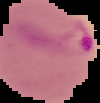
preparation = thin blood smear
image type = cell region segmented out of the field of view; surrounding area masked to black
image size = 100×103 pixels
result = Plasmodium parasites detected